Report the malaria status of this cell.
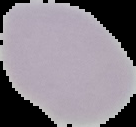

Uninfected.

Summary:
  - Image size: 136×127 pixels
  - Preparation: thin blood smear
  - Image type: segmented cell region on a black background